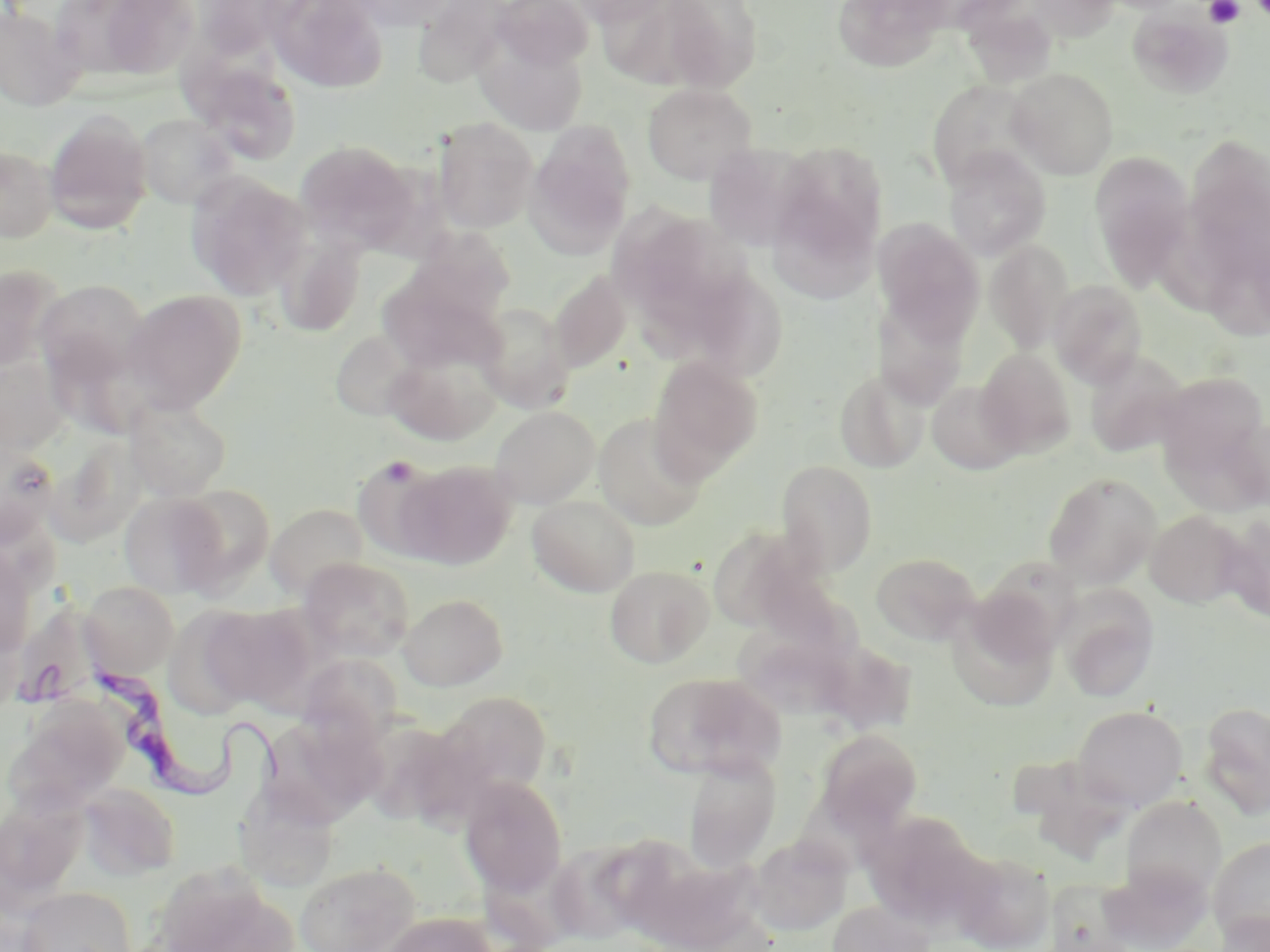 Approximate bounding boxes as [x1, y1, x2, y2] in pixels. Uninfected red blood cell locations: [268, 0, 390, 94], [343, 0, 459, 32], [491, 0, 595, 71], [565, 0, 673, 26], [656, 0, 763, 92], [831, 0, 952, 72], [1020, 0, 1123, 44], [1101, 0, 1195, 14], [88, 1, 201, 81], [413, 1, 517, 87], [956, 2, 1059, 83], [0, 5, 86, 112], [1126, 6, 1235, 99], [474, 31, 589, 135], [190, 58, 302, 165], [1007, 67, 1119, 179], [926, 79, 1040, 189], [642, 83, 757, 185], [44, 110, 153, 234], [135, 113, 240, 210], [432, 118, 539, 234], [525, 121, 637, 257], [1186, 135, 1269, 262], [295, 139, 420, 252], [767, 139, 888, 287], [0, 145, 58, 242], [943, 146, 1051, 260], [1089, 151, 1196, 292], [186, 172, 311, 299], [609, 193, 707, 319], [1156, 201, 1236, 312], [873, 218, 984, 343], [402, 231, 517, 338], [272, 232, 366, 336], [985, 241, 1075, 352], [0, 267, 68, 371], [377, 269, 504, 373], [548, 272, 633, 372], [703, 275, 789, 385], [34, 279, 151, 390], [1049, 280, 1147, 387], [123, 289, 245, 413], [876, 295, 972, 409], [474, 303, 575, 412], [331, 329, 419, 421], [383, 346, 502, 446], [976, 348, 1077, 458], [1082, 349, 1189, 457], [1, 353, 71, 454], [648, 356, 763, 480], [834, 367, 929, 472], [1155, 371, 1268, 475], [927, 380, 1025, 475], [124, 396, 232, 500], [491, 406, 599, 508], [593, 413, 709, 530], [1219, 417, 1270, 511], [0, 441, 59, 544], [352, 456, 452, 562], [776, 460, 879, 576], [394, 461, 517, 571], [1043, 472, 1162, 588], [170, 484, 275, 593], [119, 490, 231, 600], [527, 495, 641, 596], [265, 503, 369, 599], [1145, 510, 1246, 608], [1219, 516, 1270, 622], [705, 523, 817, 631], [0, 545, 36, 658], [871, 552, 981, 645], [299, 557, 415, 662], [604, 564, 715, 668], [80, 580, 179, 677], [1056, 586, 1160, 702], [400, 593, 508, 690], [946, 601, 1061, 714], [200, 604, 315, 709], [162, 605, 265, 720], [0, 614, 24, 716], [724, 626, 855, 726], [298, 653, 403, 750], [642, 671, 783, 781], [434, 690, 552, 801], [5, 702, 130, 816], [1199, 702, 1270, 817], [1072, 705, 1187, 810], [269, 723, 385, 832], [815, 728, 923, 833], [683, 752, 782, 871], [460, 776, 568, 896], [77, 783, 182, 880], [233, 785, 341, 892], [1120, 796, 1226, 901], [862, 813, 986, 933], [748, 834, 852, 936], [1208, 836, 1270, 947], [548, 840, 653, 945], [949, 848, 1057, 952], [295, 861, 421, 952], [156, 869, 297, 952], [18, 886, 136, 952], [826, 900, 935, 952], [1212, 911, 1269, 952], [377, 912, 498, 952]. Trypanosoma brucei locations: [82, 665, 295, 814]. Platelet locations: [1204, 0, 1244, 28], [1250, 0, 1270, 21], [377, 458, 420, 485]. Slide-level diagnosis: Trypanosoma brucei. Captured at 1000x magnification. Image is 1270×952 pixels. Single field of view. Thin blood film. Light microscopy. May-Grünwald-Giemsa-stained preparation.